Assess this cell for malaria.
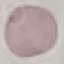

Uninfected.

Thin smear of blood. Giemsa-stained preparation. Automatically extracted cell patch, resized to 64 × 64 pixels. Photographed with a smartphone camera at the microscope eyepiece.